Assess this cell for malaria.
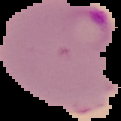

Parasitized.

Segmented cell region on a black background. Image is 121×121 pixels. From a thin blood smear.